Outline each blood parasite and name the species.
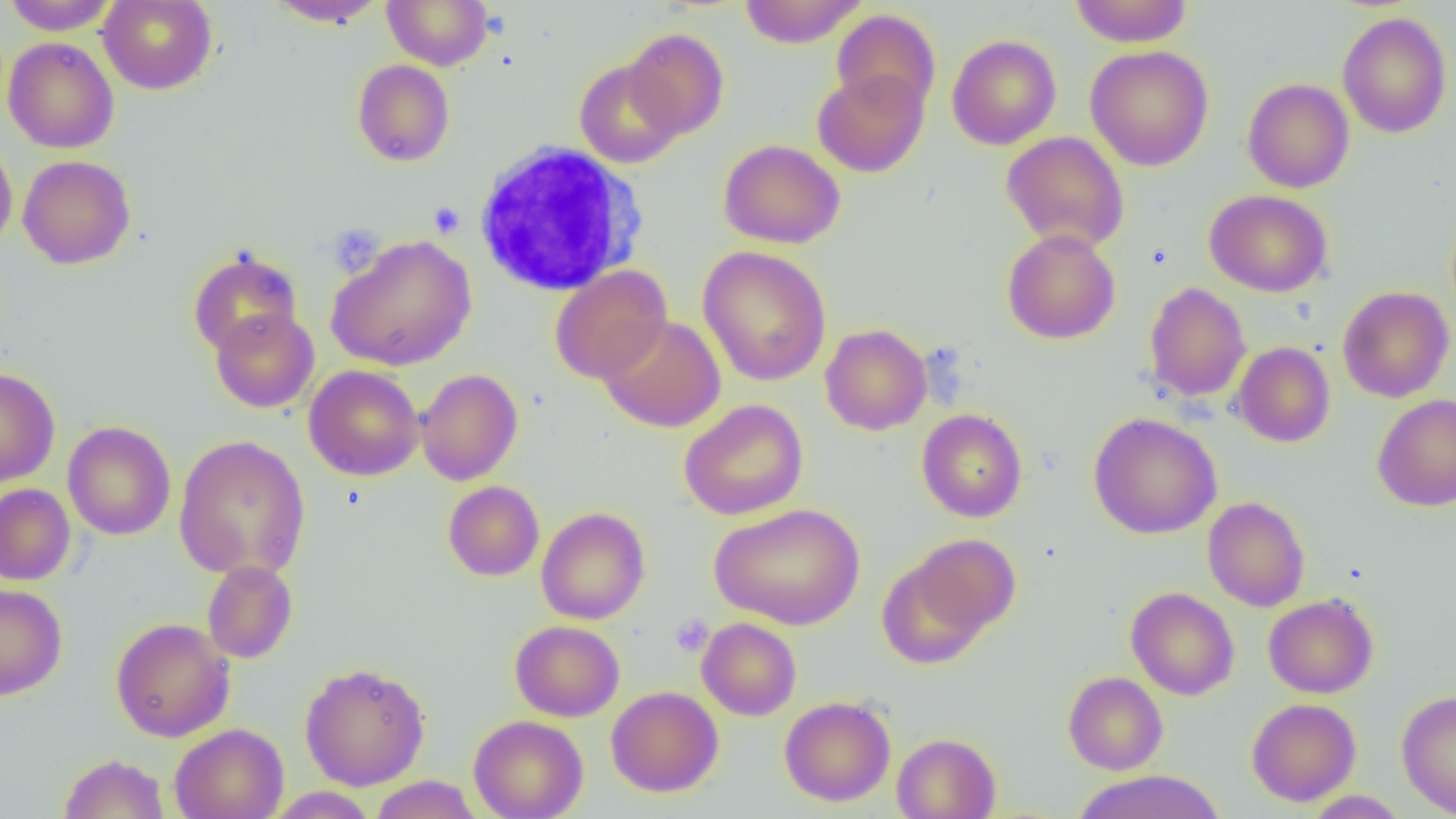

No blood parasites seen.

Summary:
  - Coordinate format: approximate bounding boxes as [x1, y1, x2, y2] in pixels
  - White blood cell locations: [473, 142, 648, 296]
  - Uninfected red blood cell locations: [2, 0, 119, 35], [98, 0, 217, 95], [267, 0, 388, 28], [382, 0, 494, 70], [738, 0, 867, 48], [1069, 0, 1194, 47], [832, 9, 941, 115], [1337, 11, 1453, 138], [624, 28, 729, 139], [947, 35, 1061, 150], [3, 37, 119, 154], [1085, 45, 1214, 171], [352, 59, 455, 166], [574, 59, 685, 168], [812, 69, 928, 177], [1242, 78, 1354, 193], [1000, 131, 1130, 252], [0, 137, 17, 256], [719, 139, 845, 249], [17, 155, 135, 269], [1205, 189, 1333, 297], [1001, 229, 1121, 344], [326, 234, 476, 371], [697, 245, 832, 387], [187, 247, 303, 357], [549, 265, 671, 384], [1144, 282, 1251, 402], [1338, 286, 1454, 403], [209, 308, 319, 413], [598, 315, 726, 432], [820, 324, 932, 435], [1232, 342, 1335, 447], [304, 365, 424, 481], [0, 368, 60, 487], [416, 369, 523, 485], [1372, 393, 1456, 512], [679, 399, 809, 520], [916, 409, 1028, 522], [1088, 412, 1222, 539], [62, 421, 176, 540], [173, 434, 311, 581], [443, 480, 544, 581], [0, 483, 75, 585], [1202, 496, 1310, 612], [709, 504, 867, 629], [536, 506, 650, 625], [905, 534, 1021, 641], [876, 552, 997, 670], [202, 561, 298, 663], [0, 583, 67, 700], [1126, 587, 1239, 700], [1263, 594, 1379, 698], [110, 617, 235, 742], [697, 617, 801, 720], [510, 620, 625, 721], [300, 662, 430, 790], [1063, 671, 1168, 775], [606, 686, 723, 797], [1396, 690, 1456, 817], [779, 695, 896, 806], [1247, 698, 1361, 805], [469, 714, 588, 819], [170, 723, 288, 819], [891, 732, 1001, 819], [58, 753, 170, 818], [1071, 770, 1225, 819], [369, 775, 483, 819], [266, 787, 377, 818], [1303, 790, 1410, 818]
  - Platelet locations: [429, 201, 465, 238], [327, 224, 384, 278], [671, 614, 713, 657]
  - Slide-level diagnosis: negative for blood parasites
  - Modality: optical microscopy
  - Preparation: thin blood smear
  - Image size: 1456×819 pixels
  - Magnification: 1000x
  - Field of view: one of a larger specimen